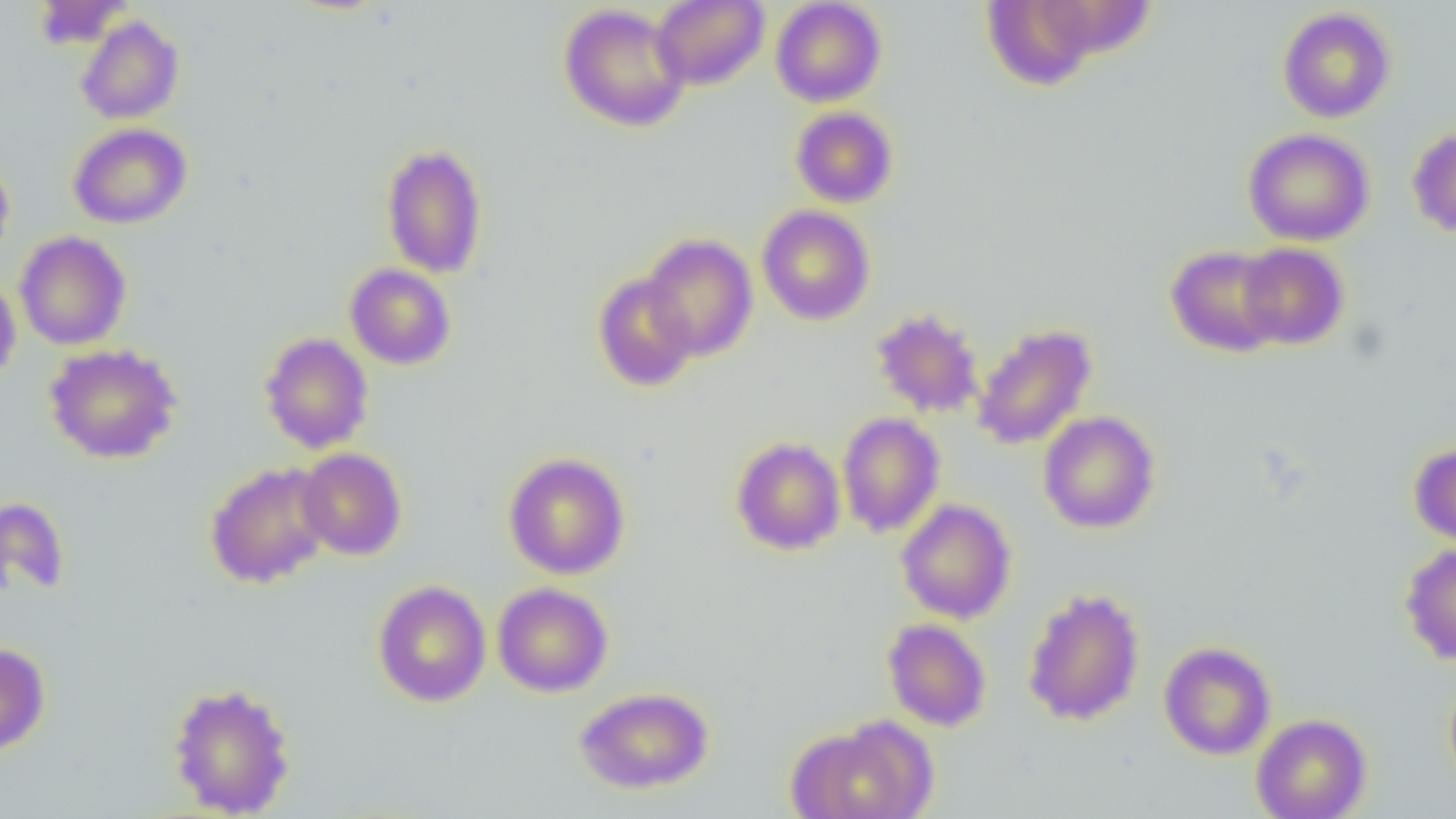

Summary:
  - Coordinate format: approximate bounding boxes as (x1,y1)-(x2,y2) corner pairs in pixels
  - Uninfected red blood cell locations: (33,0)-(133,49), (651,0)-(769,89), (770,0)-(887,107), (979,1)-(1110,90), (557,3)-(691,132), (1277,7)-(1396,123), (76,15)-(184,124), (791,107)-(898,208), (68,123)-(192,229), (1407,127)-(1456,238), (1243,128)-(1375,246), (380,143)-(488,279), (0,153)-(15,264), (757,205)-(875,326), (14,231)-(132,350), (641,233)-(758,361), (1237,243)-(1349,350), (1166,245)-(1286,357), (344,264)-(456,370), (593,272)-(699,392), (0,276)-(21,385), (870,308)-(984,418), (972,323)-(1096,450), (260,332)-(374,454), (44,343)-(182,464), (1038,411)-(1161,534), (837,412)-(945,538), (731,437)-(846,556), (1409,443)-(1456,549), (296,448)-(407,560), (503,452)-(631,579), (205,461)-(334,588), (0,498)-(70,598), (896,499)-(1016,623), (1400,543)-(1456,665), (373,580)-(492,707), (492,582)-(614,697), (1023,588)-(1145,726), (882,618)-(992,731), (1159,641)-(1276,760), (0,642)-(51,756), (1444,671)-(1456,793), (166,682)-(297,817), (574,687)-(714,794), (1251,713)-(1372,819), (786,720)-(935,819)
  - Slide-level diagnosis: negative for blood parasites
  - Modality: optical microscopy
  - Field of view: single
  - Image size: 1456×819 pixels
  - Magnification: 1000x
  - Preparation: thin blood smear